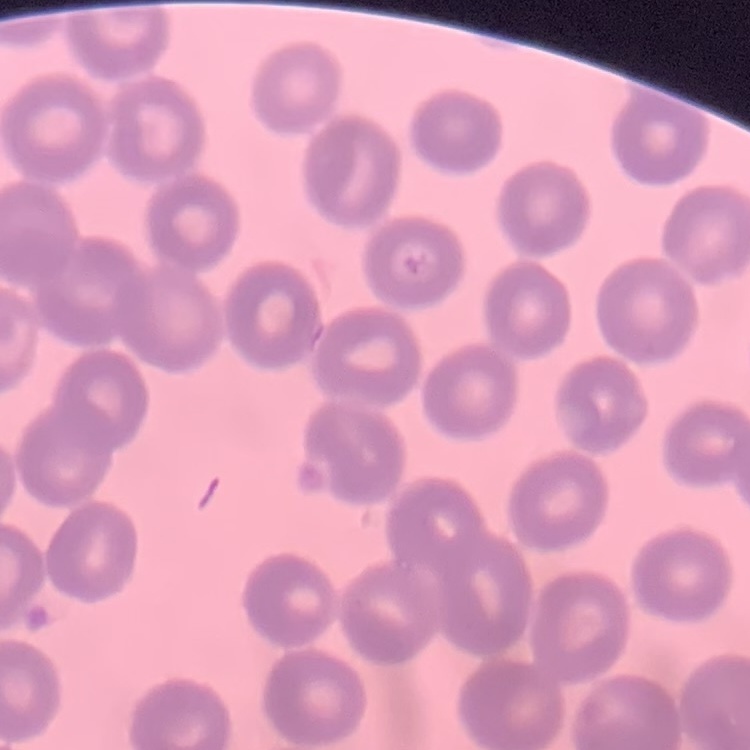

Summary:
  - Erythrocyte morphology: no rouleaux formation
  - Stain: Field's or Giemsa
  - Preparation: thin blood smear
  - Image type: one tile cut from a larger photomicrograph